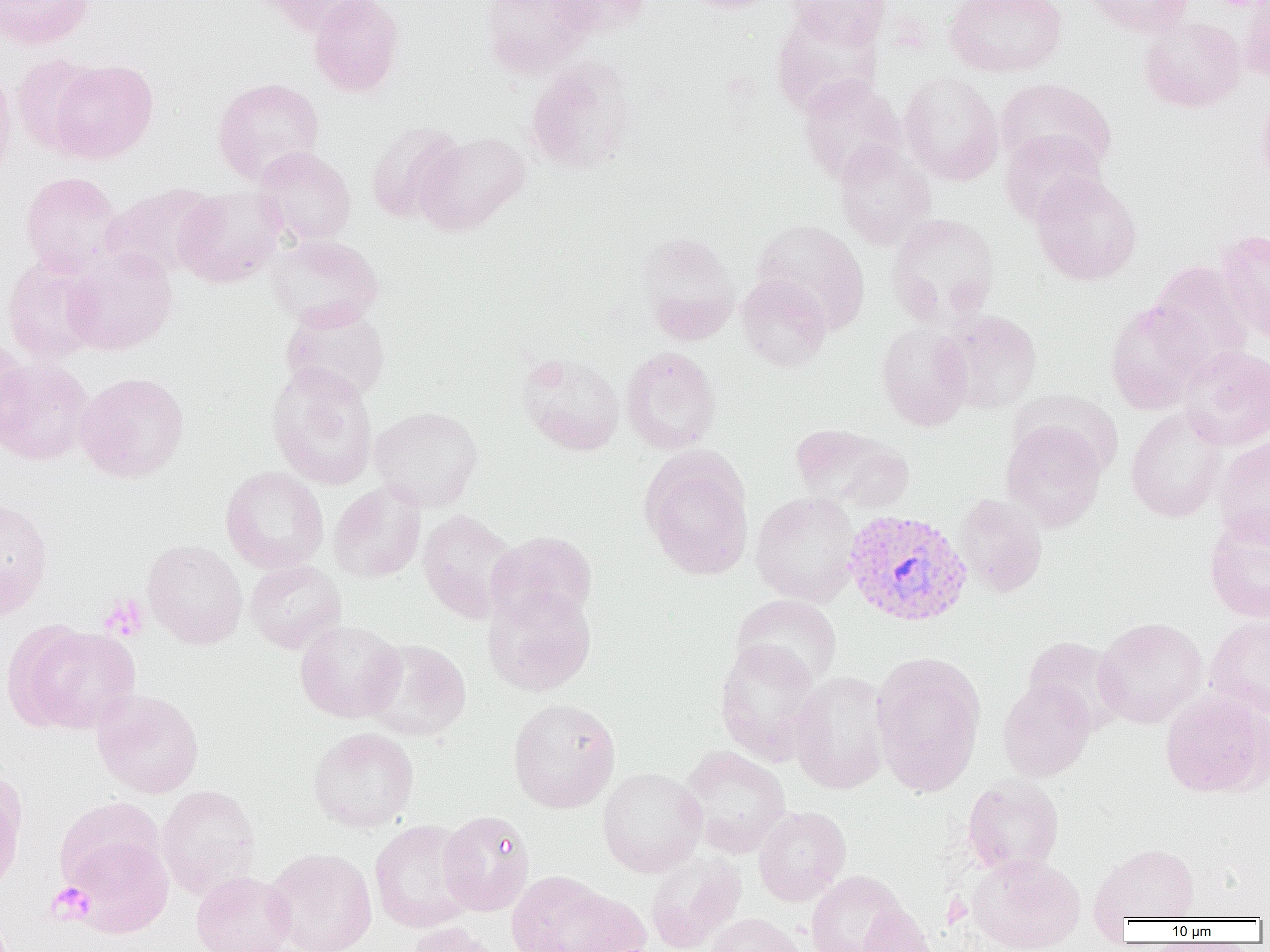

Summary:
  - Coordinate format: approximate bounding boxes as named x1/y1/x2/y2 corners in pixels
  - Platelet locations: (x1=99, y1=594, x2=149, y2=641), (x1=47, y1=882, x2=95, y2=923)
  - Plasmodium vivax-infected red blood cell locations: (x1=843, y1=509, x2=972, y2=627)
  - Uninfected red blood cell locations: (x1=0, y1=0, x2=94, y2=50), (x1=258, y1=0, x2=377, y2=36), (x1=308, y1=0, x2=405, y2=97), (x1=479, y1=0, x2=598, y2=78), (x1=547, y1=0, x2=654, y2=38), (x1=676, y1=0, x2=783, y2=14), (x1=786, y1=0, x2=891, y2=49), (x1=944, y1=0, x2=1067, y2=78), (x1=1082, y1=0, x2=1195, y2=37), (x1=1239, y1=1, x2=1269, y2=84), (x1=770, y1=8, x2=883, y2=116), (x1=1139, y1=15, x2=1246, y2=113), (x1=10, y1=53, x2=103, y2=156), (x1=524, y1=57, x2=637, y2=175), (x1=49, y1=59, x2=159, y2=163), (x1=0, y1=63, x2=16, y2=185), (x1=899, y1=72, x2=1004, y2=186), (x1=797, y1=74, x2=906, y2=186), (x1=213, y1=77, x2=324, y2=185), (x1=995, y1=78, x2=1117, y2=178), (x1=1256, y1=89, x2=1270, y2=189), (x1=364, y1=120, x2=465, y2=224), (x1=999, y1=130, x2=1107, y2=227), (x1=413, y1=131, x2=531, y2=236), (x1=833, y1=140, x2=936, y2=250), (x1=253, y1=146, x2=357, y2=246), (x1=20, y1=171, x2=124, y2=277), (x1=1031, y1=173, x2=1142, y2=284), (x1=100, y1=182, x2=220, y2=281), (x1=174, y1=187, x2=286, y2=288), (x1=886, y1=214, x2=1000, y2=329), (x1=751, y1=220, x2=870, y2=334), (x1=1216, y1=229, x2=1270, y2=345), (x1=636, y1=231, x2=740, y2=343), (x1=267, y1=234, x2=383, y2=331), (x1=63, y1=247, x2=178, y2=356), (x1=2, y1=255, x2=104, y2=363), (x1=1145, y1=261, x2=1255, y2=378), (x1=736, y1=274, x2=832, y2=372), (x1=1105, y1=299, x2=1211, y2=414), (x1=280, y1=305, x2=391, y2=404), (x1=939, y1=310, x2=1042, y2=414), (x1=876, y1=321, x2=974, y2=431), (x1=1, y1=337, x2=31, y2=447), (x1=621, y1=346, x2=723, y2=455), (x1=1176, y1=346, x2=1270, y2=450), (x1=516, y1=352, x2=626, y2=456), (x1=0, y1=357, x2=96, y2=466), (x1=266, y1=361, x2=379, y2=489), (x1=76, y1=371, x2=190, y2=483), (x1=1011, y1=389, x2=1122, y2=479), (x1=369, y1=405, x2=484, y2=510), (x1=1126, y1=407, x2=1228, y2=522), (x1=1000, y1=419, x2=1107, y2=532), (x1=791, y1=423, x2=913, y2=513), (x1=1213, y1=434, x2=1270, y2=546), (x1=640, y1=451, x2=754, y2=581), (x1=220, y1=466, x2=329, y2=574), (x1=328, y1=481, x2=426, y2=583), (x1=750, y1=492, x2=861, y2=607), (x1=954, y1=493, x2=1048, y2=597), (x1=0, y1=496, x2=53, y2=619), (x1=417, y1=508, x2=521, y2=624), (x1=1204, y1=513, x2=1270, y2=623), (x1=486, y1=530, x2=598, y2=627), (x1=142, y1=540, x2=248, y2=649), (x1=245, y1=559, x2=346, y2=653), (x1=482, y1=586, x2=597, y2=697), (x1=731, y1=594, x2=842, y2=689), (x1=1204, y1=615, x2=1270, y2=720), (x1=1094, y1=617, x2=1208, y2=727), (x1=295, y1=620, x2=405, y2=723), (x1=15, y1=624, x2=143, y2=735), (x1=1023, y1=635, x2=1128, y2=734), (x1=362, y1=638, x2=472, y2=741), (x1=715, y1=639, x2=824, y2=765), (x1=872, y1=654, x2=985, y2=797), (x1=875, y1=667, x2=1098, y2=789), (x1=789, y1=670, x2=891, y2=795), (x1=998, y1=678, x2=1096, y2=782), (x1=92, y1=689, x2=204, y2=799), (x1=1160, y1=690, x2=1269, y2=799), (x1=507, y1=697, x2=621, y2=813), (x1=307, y1=726, x2=420, y2=832), (x1=679, y1=744, x2=792, y2=857), (x1=597, y1=766, x2=707, y2=877), (x1=0, y1=767, x2=27, y2=895), (x1=962, y1=775, x2=1064, y2=876), (x1=156, y1=785, x2=260, y2=900), (x1=53, y1=797, x2=166, y2=892), (x1=753, y1=806, x2=852, y2=906), (x1=438, y1=810, x2=535, y2=916), (x1=369, y1=819, x2=478, y2=933), (x1=64, y1=835, x2=174, y2=937), (x1=1089, y1=843, x2=1200, y2=924), (x1=265, y1=847, x2=377, y2=952), (x1=645, y1=851, x2=747, y2=951), (x1=968, y1=854, x2=1086, y2=952), (x1=805, y1=870, x2=912, y2=952), (x1=190, y1=871, x2=296, y2=952), (x1=506, y1=871, x2=634, y2=952), (x1=859, y1=904, x2=940, y2=952), (x1=707, y1=913, x2=805, y2=952), (x1=406, y1=922, x2=511, y2=952)
  - Slide-level diagnosis: Plasmodium vivax
  - Field of view: one of a larger specimen
  - Image size: 1270×952 pixels
  - Modality: optical microscopy
  - Magnification: 1000x
  - Preparation: thin blood film